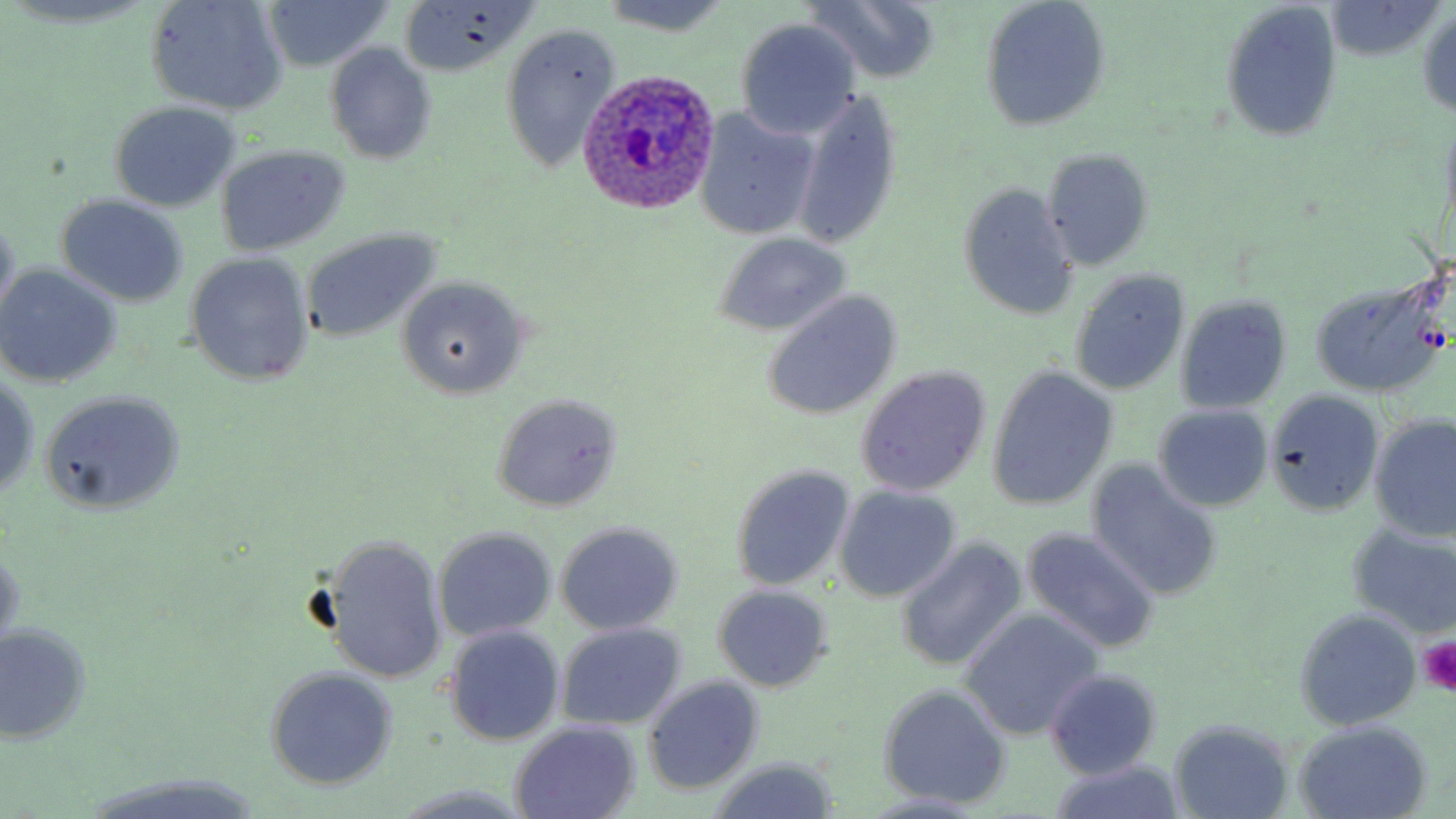

Summary:
  - Coordinate format: approximate bounding boxes as (x1, y1, x2, y2) in pixels
  - Plasmodium ovale-infected red blood cell locations: (575, 67, 722, 218)
  - Platelet locations: (1417, 637, 1456, 693)
  - Uninfected red blood cell locations: (4, 0, 156, 31), (145, 0, 289, 116), (262, 0, 393, 73), (804, 0, 945, 84), (978, 0, 1112, 133), (400, 1, 540, 77), (1219, 1, 1342, 144), (600, 2, 732, 37), (1325, 2, 1446, 62), (1416, 8, 1456, 116), (733, 18, 862, 138), (498, 22, 622, 172), (323, 42, 439, 166), (792, 89, 902, 249), (109, 103, 242, 213), (694, 108, 819, 240), (215, 144, 353, 255), (1040, 149, 1154, 270), (957, 181, 1081, 322), (56, 196, 189, 307), (0, 210, 19, 321), (299, 228, 441, 345), (711, 233, 853, 336), (184, 251, 315, 388), (0, 265, 122, 388), (1069, 268, 1190, 397), (1308, 275, 1449, 399), (397, 277, 534, 397), (761, 290, 903, 421), (1175, 295, 1293, 415), (854, 367, 990, 497), (986, 367, 1118, 513), (1, 370, 41, 503), (41, 390, 185, 513), (1265, 391, 1382, 516), (489, 393, 624, 512), (1152, 405, 1274, 512), (1370, 415, 1456, 541), (1086, 461, 1225, 601), (730, 464, 856, 591), (835, 484, 962, 603), (555, 522, 684, 636), (1345, 522, 1456, 638), (432, 527, 557, 643), (1021, 528, 1161, 654), (321, 534, 447, 685), (891, 536, 1027, 672), (0, 548, 23, 657), (712, 584, 835, 691), (1293, 608, 1422, 730), (958, 609, 1104, 740), (555, 621, 687, 730), (0, 623, 93, 744), (444, 624, 565, 746), (264, 666, 398, 792), (1043, 668, 1163, 779), (641, 674, 765, 796), (877, 684, 1013, 808), (1167, 717, 1295, 818), (1291, 720, 1434, 817), (510, 721, 642, 819), (704, 757, 841, 819), (1045, 760, 1188, 819), (82, 772, 269, 817), (390, 784, 538, 818), (857, 792, 989, 818)
  - Slide-level diagnosis: Plasmodium ovale
  - Preparation: thin blood film
  - Field of view: one of a larger specimen
  - Modality: light microscopy
  - Stain: May-Grünwald-Giemsa
  - Magnification: 1000x
  - Image size: 1456×819 pixels